Classify this cell by malaria status.
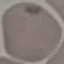

It is uninfected.

capture = smartphone through the microscope eyepiece
image type = cell patch, automatically extracted from a larger field of view and resized to 64 × 64 pixels
preparation = thin blood smear
stain = Giemsa